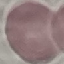

Summary:
  - Result: no malaria parasites seen
  - Stain: Giemsa
  - Capture: smartphone through the microscope eyepiece
  - Image type: cell patch, automatically extracted from a larger field of view and resized to 64 × 64 pixels
  - Preparation: thin smear